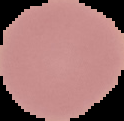

image type = cell region segmented out of the field of view; surrounding area masked to black
preparation = thin blood film
image size = 124×121 pixels
result = no malaria parasites detected